Report the malaria status of this cell.
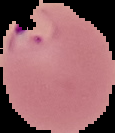
Parasitized.

image type = segmented cell region with the area outside set to black
image size = 115×133 pixels
preparation = thin blood film